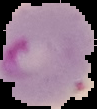

malaria status = parasitized
image type = segmented cell region on a black background
image size = 97×109 pixels
preparation = thin blood film